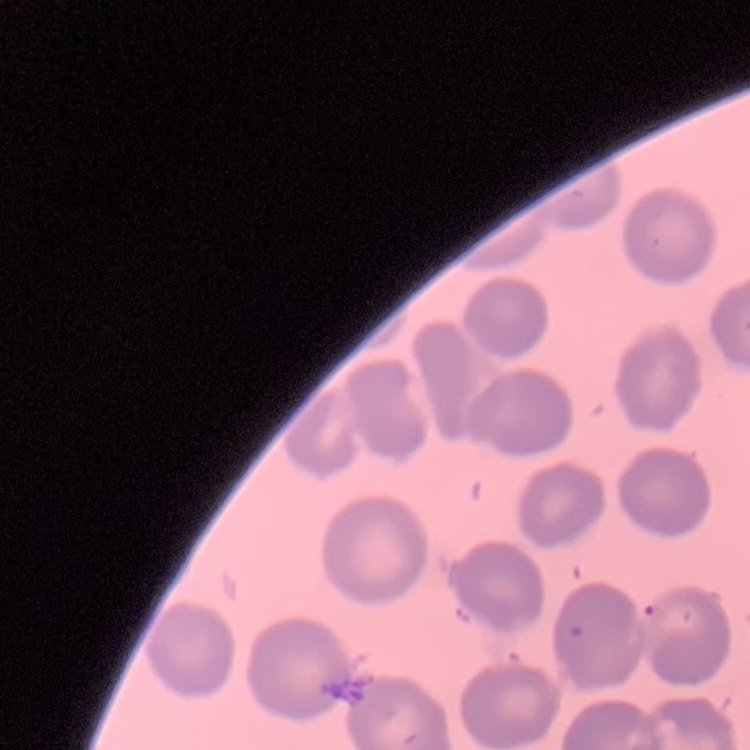
Summary:
  - Red blood cell morphology: no rouleaux formation
  - Preparation: thin blood film
  - Stain: Field's or Giemsa
  - Image type: square crop of a larger photomicrograph